Assess the morphology of the erythrocytes.
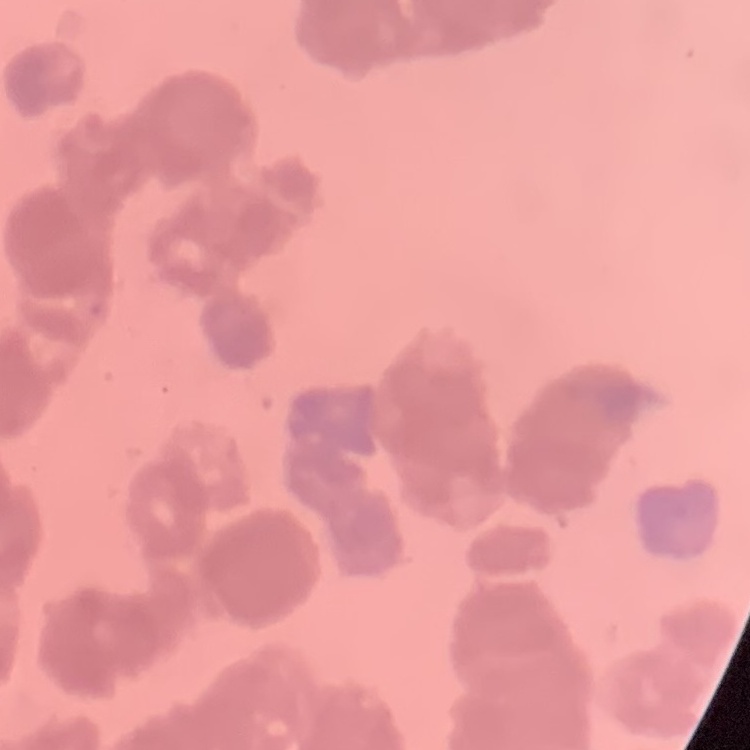
They show rouleaux formation.

Summary:
  - Preparation: thin blood film
  - Stain: Field's or Giemsa
  - Image type: square crop of a larger photomicrograph